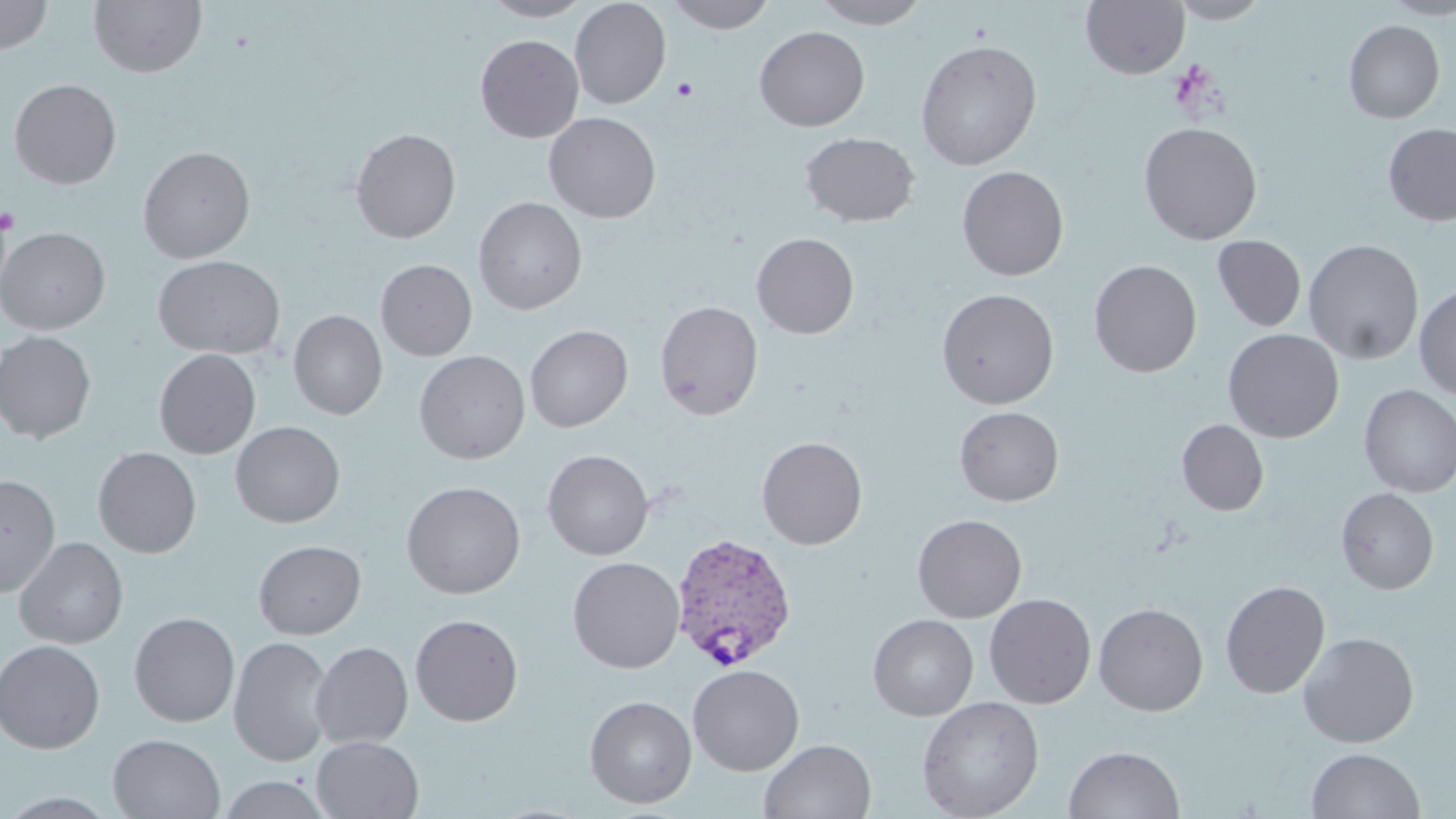
{
  "slide_level_diagnosis": "Plasmodium vivax",
  "image_size": "1456×819 pixels",
  "stain": "May-Grünwald-Giemsa",
  "plasmodium_vivax_infected_red_blood_cell_locations": "approximate bounding boxes as (x1, y1, x2, y2) in pixels: (670, 532, 798, 670)",
  "magnification": "1000x",
  "preparation": "thin blood smear",
  "platelet_locations": "approximate bounding boxes as (x1, y1, x2, y2) in pixels: (671, 75, 699, 101), (0, 208, 19, 234)",
  "modality": "light microscopy",
  "field_of_view": "single",
  "uninfected_red_blood_cell_locations": "approximate bounding boxes as (x1, y1, x2, y2) in pixels: (0, 0, 54, 56), (89, 0, 207, 78), (478, 0, 595, 22), (570, 0, 671, 109), (666, 0, 778, 33), (811, 0, 931, 29), (1167, 0, 1273, 23), (1379, 0, 1456, 19), (1081, 1, 1189, 79), (1343, 20, 1445, 123), (754, 26, 870, 131), (475, 34, 584, 142), (915, 39, 1042, 170), (9, 78, 122, 189), (544, 111, 662, 223), (1139, 122, 1262, 245), (1383, 124, 1456, 225), (350, 127, 461, 244), (799, 131, 920, 227), (137, 146, 256, 263), (956, 165, 1069, 281), (473, 197, 587, 315), (0, 227, 110, 334), (751, 232, 860, 339), (1212, 235, 1306, 332), (1303, 238, 1424, 365), (152, 254, 286, 359), (376, 259, 477, 361), (1088, 259, 1202, 377), (1414, 285, 1456, 399), (936, 288, 1059, 409), (654, 300, 763, 420), (288, 310, 387, 420), (525, 325, 633, 432), (1223, 328, 1344, 443), (0, 330, 96, 443), (154, 349, 260, 459), (414, 350, 530, 465), (1358, 385, 1456, 497), (953, 406, 1064, 506), (1177, 419, 1269, 515), (230, 421, 345, 528), (756, 436, 868, 550), (93, 446, 201, 558), (542, 449, 654, 560), (0, 474, 60, 597), (401, 480, 526, 599), (1336, 488, 1439, 595), (912, 514, 1027, 623), (14, 537, 129, 649), (253, 540, 366, 639), (567, 556, 685, 673), (1220, 580, 1330, 699), (984, 592, 1096, 709), (1093, 602, 1209, 716), (129, 612, 240, 727), (410, 613, 523, 726), (867, 614, 979, 721), (1298, 632, 1419, 748), (229, 636, 334, 767), (310, 636, 526, 741), (0, 639, 105, 753), (310, 641, 413, 749), (688, 663, 805, 775), (584, 695, 697, 809), (916, 696, 1044, 818), (107, 733, 226, 818), (311, 735, 424, 819), (759, 738, 876, 819), (1064, 745, 1185, 819), (1306, 747, 1426, 818), (216, 773, 333, 818)"
}